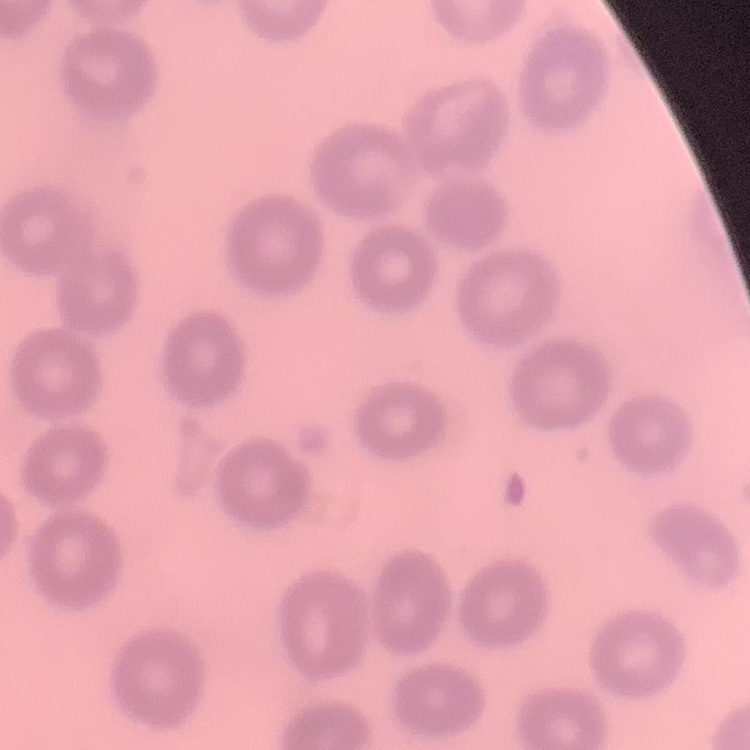

red blood cell morphology = no rouleaux formation
preparation = thin peripheral smear
stain = Field's or Giemsa
image type = square crop of a larger photomicrograph